Locate and identify every blood parasite.
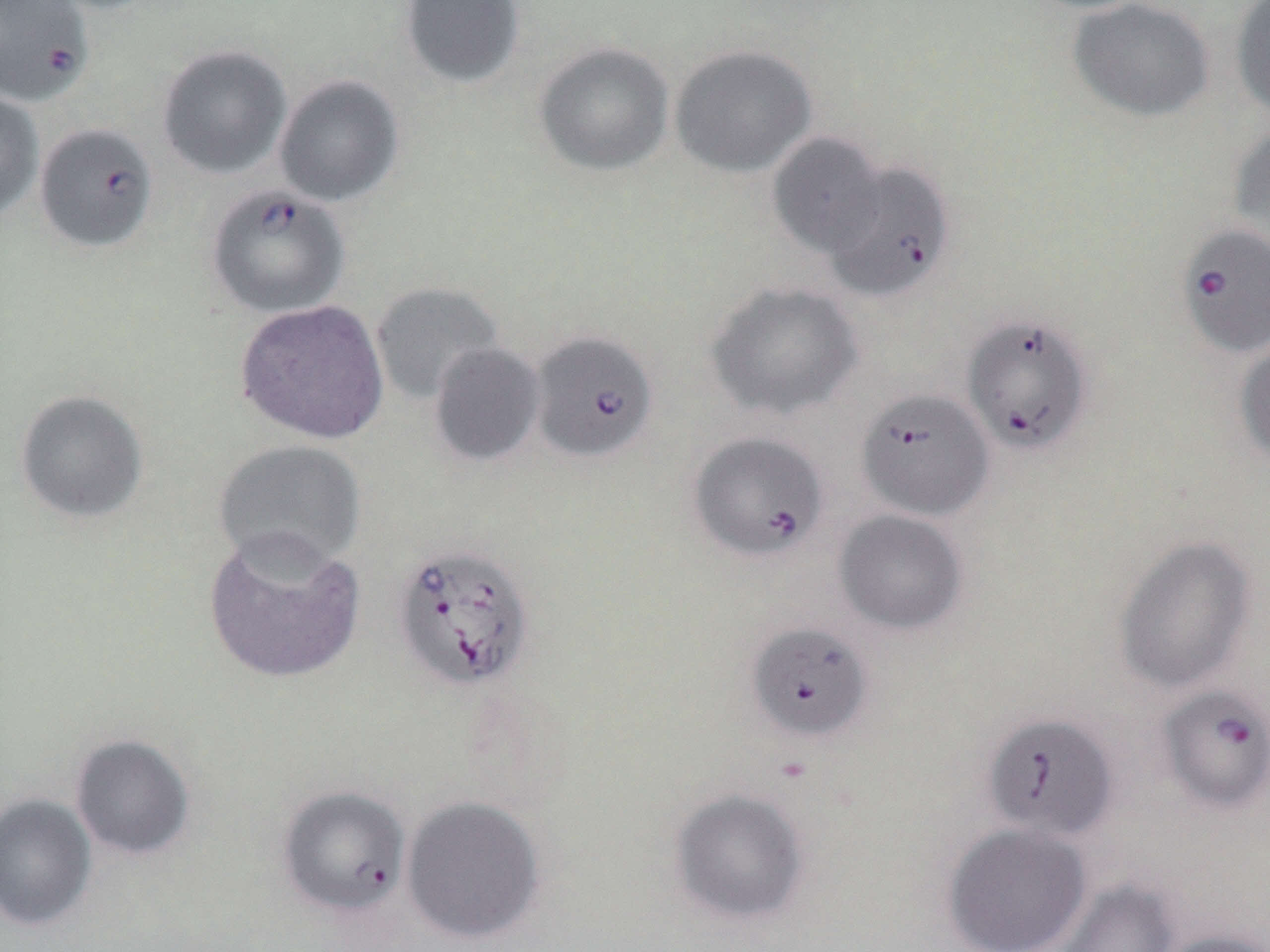

Approximate bounding boxes as named x1/y1/x2/y2 corners in pixels.
Babesia divergens-infected red blood cells: (x1=0, y1=0, x2=94, y2=106), (x1=33, y1=122, x2=160, y2=254), (x1=825, y1=159, x2=956, y2=303), (x1=205, y1=183, x2=352, y2=318), (x1=1175, y1=222, x2=1270, y2=358), (x1=961, y1=313, x2=1095, y2=457), (x1=529, y1=331, x2=659, y2=464), (x1=855, y1=387, x2=995, y2=521), (x1=688, y1=431, x2=828, y2=562), (x1=390, y1=541, x2=536, y2=694), (x1=747, y1=622, x2=873, y2=743), (x1=1156, y1=683, x2=1270, y2=814), (x1=982, y1=712, x2=1118, y2=842), (x1=276, y1=785, x2=411, y2=919).
No Plasmodium falciparum, Plasmodium ovale, Plasmodium malariae, Plasmodium vivax, or Trypanosoma brucei observed.

Summary:
  - Uninfected red blood cell locations: (x1=399, y1=0, x2=526, y2=88), (x1=1068, y1=0, x2=1216, y2=122), (x1=1230, y1=0, x2=1270, y2=120), (x1=533, y1=41, x2=675, y2=176), (x1=157, y1=43, x2=293, y2=180), (x1=669, y1=44, x2=817, y2=179), (x1=273, y1=74, x2=405, y2=207), (x1=0, y1=91, x2=44, y2=221), (x1=1228, y1=122, x2=1270, y2=249), (x1=766, y1=132, x2=891, y2=260), (x1=705, y1=281, x2=863, y2=420), (x1=370, y1=282, x2=504, y2=405), (x1=234, y1=299, x2=390, y2=445), (x1=1234, y1=334, x2=1270, y2=467), (x1=429, y1=343, x2=545, y2=468), (x1=14, y1=389, x2=149, y2=524), (x1=212, y1=439, x2=366, y2=573), (x1=833, y1=510, x2=969, y2=635), (x1=202, y1=528, x2=366, y2=686), (x1=1112, y1=534, x2=1257, y2=694), (x1=70, y1=734, x2=196, y2=861), (x1=669, y1=788, x2=810, y2=926), (x1=0, y1=793, x2=97, y2=932), (x1=401, y1=795, x2=546, y2=944), (x1=941, y1=822, x2=1091, y2=951), (x1=1054, y1=878, x2=1181, y2=952), (x1=1154, y1=929, x2=1270, y2=952)
  - Slide-level diagnosis: Babesia divergens
  - Field of view: one of a larger specimen
  - Image size: 1270×952 pixels
  - Modality: light microscopy
  - Stain: May-Grünwald-Giemsa
  - Magnification: 1000x
  - Preparation: thin blood smear